Describe the morphology of the red blood cells.
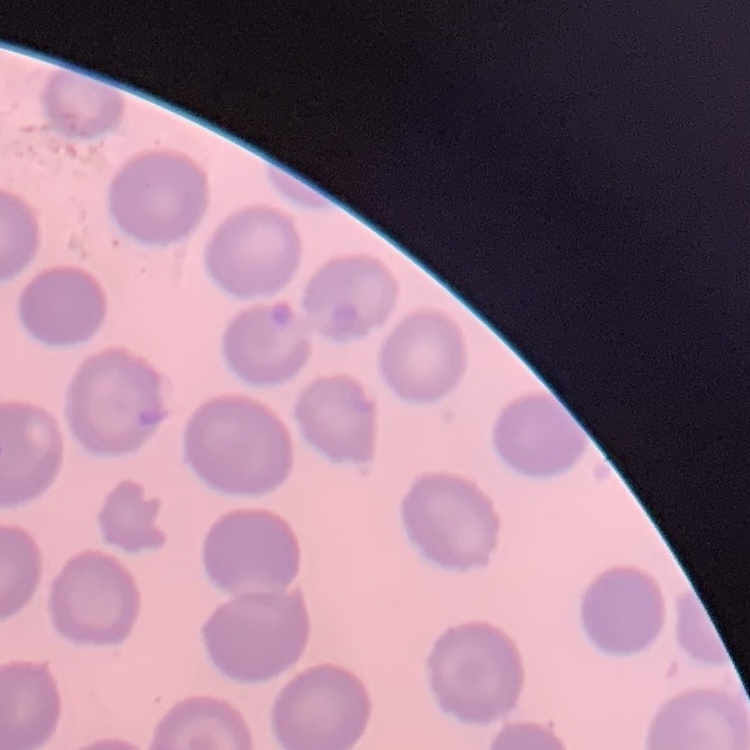

No rouleaux formation.

Summary:
  - Stain: Field's or Giemsa
  - Image type: one tile cut from a larger photomicrograph
  - Preparation: thin peripheral smear